Name the blood parasite species.
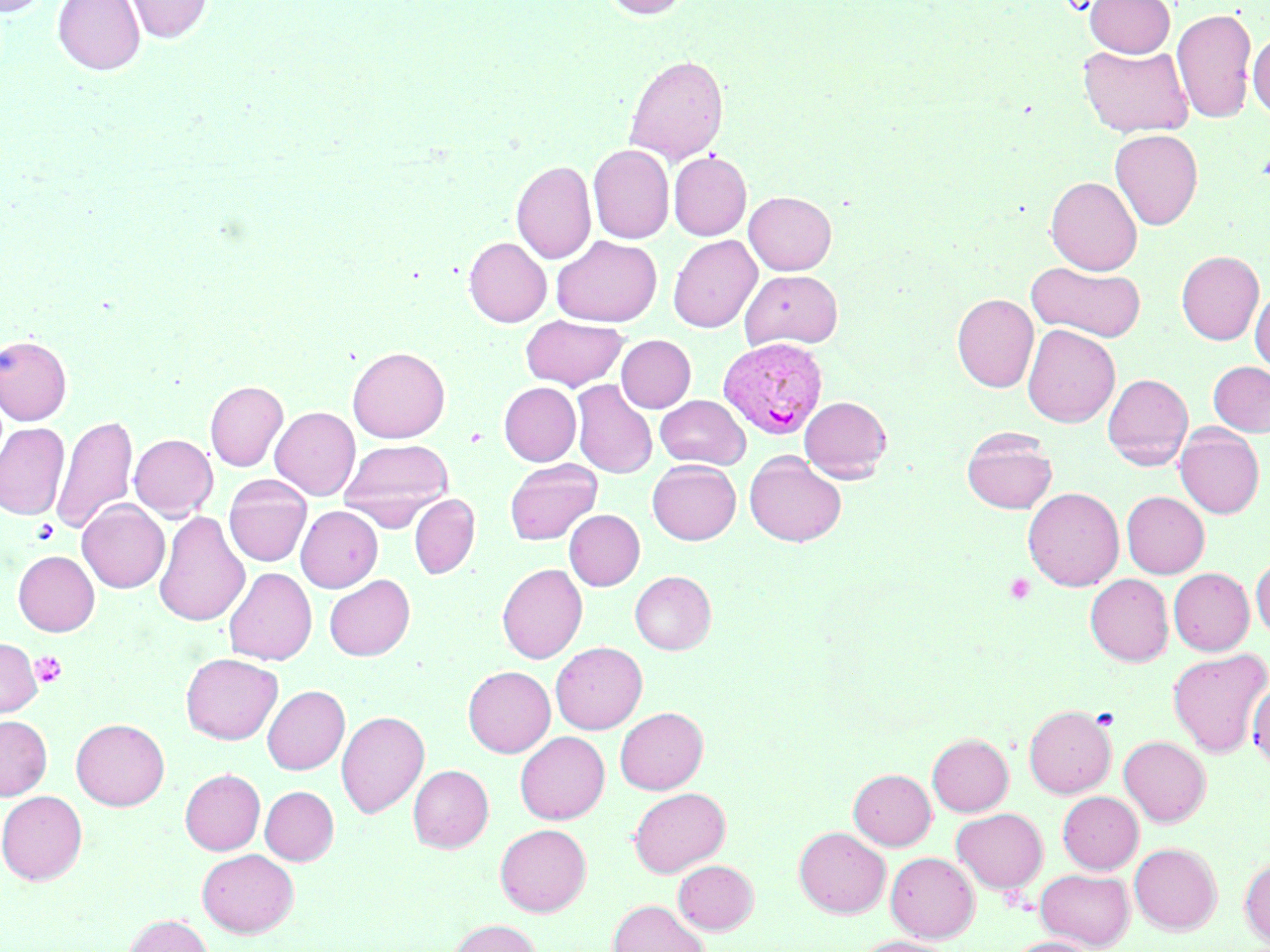
Plasmodium vivax.

platelet locations = approximate bounding boxes as (x1,y1)-(x2,y2) corner pairs in pixels: (32,519)-(59,543), (1004,573)-(1035,604), (30,651)-(67,688)
stain = May-Grünwald-Giemsa
modality = optical microscopy
preparation = thin blood smear
uninfected red blood cell locations = approximate bounding boxes as (x1,y1)-(x2,y2) corner pairs in pixels: (0,0)-(52,17), (53,0)-(144,75), (122,0)-(213,43), (602,0)-(691,18), (1085,0)-(1175,57), (1172,7)-(1257,124), (1249,30)-(1270,118), (1079,43)-(1194,137), (624,54)-(728,165), (1109,129)-(1203,230), (588,144)-(674,244), (669,151)-(751,240), (511,160)-(596,264), (1045,176)-(1142,275), (744,191)-(836,275), (668,234)-(762,333), (551,235)-(662,327), (464,237)-(551,327), (1176,250)-(1264,344), (1027,261)-(1145,342), (740,269)-(843,350), (1250,287)-(1270,376), (952,293)-(1038,392), (520,315)-(627,390), (1022,324)-(1120,427), (0,335)-(72,425), (616,335)-(696,413), (347,346)-(450,443), (1208,361)-(1270,436), (1103,373)-(1193,470), (205,380)-(288,471), (571,380)-(656,478), (499,382)-(581,466), (654,395)-(750,468), (800,396)-(891,482), (270,406)-(360,500), (52,416)-(138,534), (0,422)-(69,520), (1174,426)-(1264,518), (961,428)-(1057,514), (129,434)-(218,521), (339,438)-(453,528), (744,453)-(847,547), (504,459)-(602,545), (647,459)-(741,545), (223,475)-(312,567), (1023,487)-(1124,591), (1121,491)-(1209,578), (409,494)-(480,579), (77,500)-(170,593), (296,505)-(383,592), (564,509)-(644,591), (154,511)-(249,627), (13,550)-(99,636), (1251,555)-(1270,638), (497,563)-(587,663), (224,567)-(316,665), (1168,568)-(1254,655), (630,571)-(716,654), (324,574)-(415,661), (1085,574)-(1174,665), (0,638)-(41,717), (551,641)-(647,734), (1168,648)-(1269,756), (181,653)-(282,744), (463,666)-(555,757), (1247,681)-(1270,768), (262,685)-(349,774), (1024,705)-(1116,798), (615,707)-(707,794), (336,710)-(429,818), (0,715)-(52,800), (71,718)-(169,810), (515,731)-(609,824), (927,733)-(1013,816), (1119,736)-(1211,826), (408,765)-(493,852), (848,768)-(935,849), (180,769)-(265,855), (260,786)-(339,865), (629,787)-(730,876), (0,791)-(88,884), (1057,791)-(1143,873), (951,807)-(1047,894), (495,823)-(591,916), (794,827)-(890,917), (1129,843)-(1221,934), (197,848)-(299,937), (886,852)-(979,942), (1240,857)-(1270,946), (674,860)-(758,934), (1035,868)-(1134,950), (608,900)-(709,952), (123,914)-(213,952), (448,919)-(541,952), (852,936)-(956,952), (1006,936)-(1097,952)
image size = 1270×952 pixels
magnification = 1000x
field of view = one of a larger specimen
Plasmodium vivax-infected red blood cell locations = approximate bounding boxes as (x1,y1)-(x2,y2) corner pairs in pixels: (717,337)-(829,440)